Give the extent of all white blood cells.
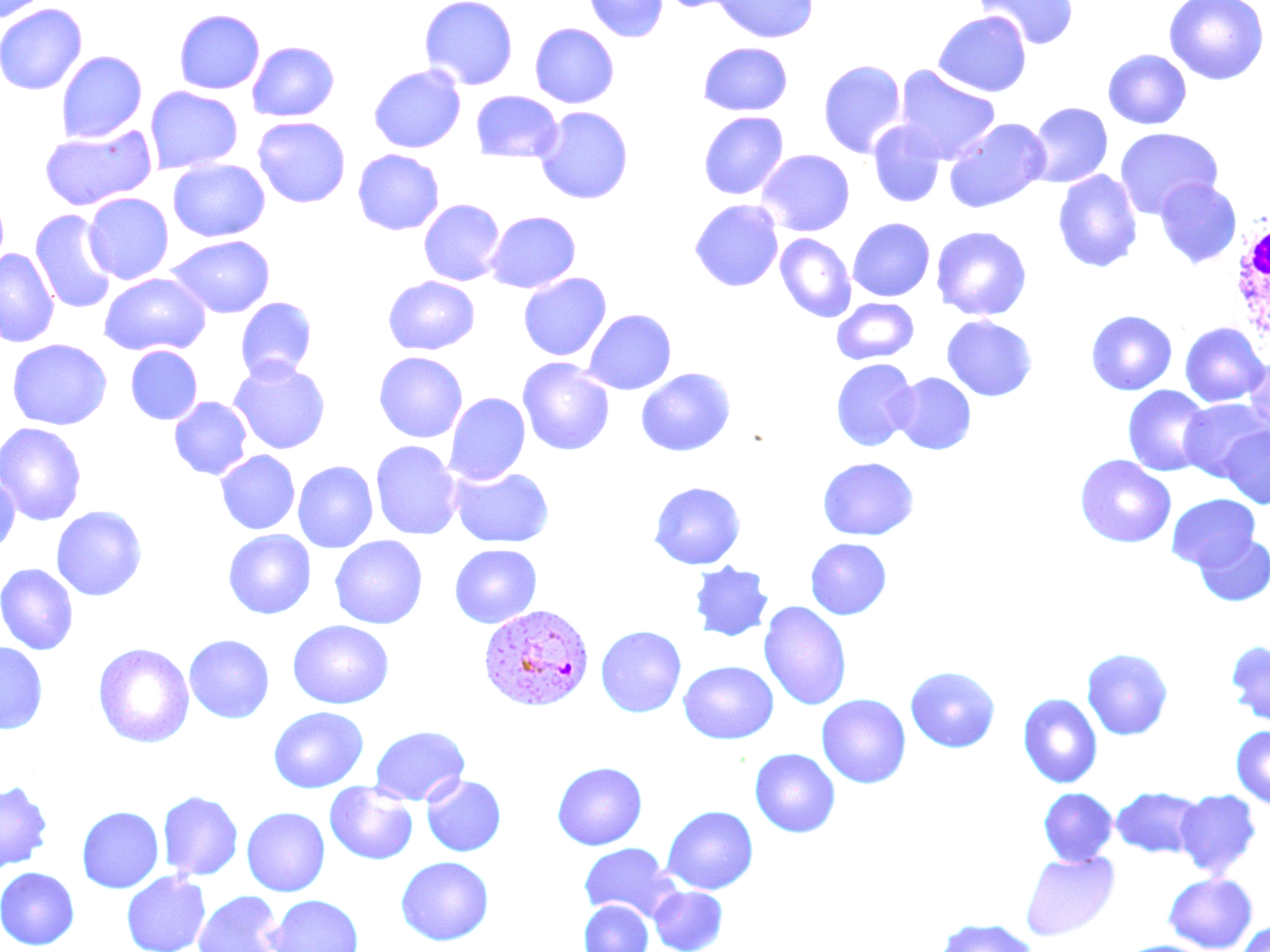

Approximate bounding boxes as (x1,y1)-(x2,y2) corner pairs in pixels.
White blood cells: (1231,212)-(1270,349).

Plasmodium vivax-infected red blood cell locations: (478,605)-(595,714). Uninfected red blood cell locations: (1,0)-(51,24), (420,0)-(518,90), (583,0)-(669,42), (656,0)-(750,13), (712,0)-(819,43), (974,0)-(1080,50), (1164,0)-(1268,86), (0,4)-(88,95), (173,9)-(265,95), (933,11)-(1032,97), (529,23)-(620,108), (247,41)-(340,121), (698,42)-(793,116), (1103,49)-(1192,130), (56,50)-(147,143), (818,60)-(907,159), (368,64)-(466,153), (894,65)-(1001,165), (145,86)-(243,174), (471,90)-(562,161), (1027,102)-(1113,188), (534,106)-(634,205), (698,111)-(789,200), (252,116)-(350,208), (944,117)-(1051,213), (867,121)-(946,208), (39,125)-(157,211), (1115,127)-(1222,220), (352,149)-(445,235), (756,149)-(855,236), (168,159)-(270,242), (1052,169)-(1143,273), (1155,178)-(1242,268), (83,193)-(173,283), (419,199)-(505,286), (689,199)-(784,292), (30,210)-(117,314), (485,210)-(581,294), (848,217)-(935,301), (931,225)-(1032,321), (775,233)-(857,322), (166,235)-(275,319), (0,249)-(59,348), (518,272)-(612,361), (98,273)-(211,357), (384,276)-(480,355), (235,297)-(317,381), (832,298)-(919,365), (582,309)-(676,395), (1086,310)-(1177,395), (941,315)-(1038,402), (1179,322)-(1269,407), (7,338)-(112,430), (126,346)-(203,425), (373,351)-(468,443), (1243,354)-(1270,441), (517,358)-(614,456), (830,358)-(919,451), (229,359)-(331,455), (636,367)-(736,457), (890,372)-(976,455), (1123,386)-(1213,477), (445,393)-(530,485), (170,396)-(252,480), (1179,397)-(1269,482), (0,422)-(87,526), (1219,425)-(1270,509), (370,440)-(462,540), (215,450)-(300,534), (1074,454)-(1176,548), (817,456)-(919,541), (293,460)-(379,553), (449,466)-(554,548), (0,469)-(20,556), (649,481)-(746,569), (1167,494)-(1260,570), (51,505)-(147,601), (223,529)-(315,619), (1194,532)-(1270,606), (329,536)-(428,629), (805,538)-(892,620), (449,544)-(542,628), (688,561)-(774,641), (1,563)-(78,655), (758,601)-(852,711), (288,620)-(394,709), (595,625)-(686,717), (184,634)-(274,724), (0,641)-(49,735), (1226,641)-(1270,725), (93,642)-(195,749), (1081,648)-(1174,741), (678,661)-(778,744), (905,665)-(1001,753), (816,694)-(911,788), (1018,694)-(1103,789), (268,706)-(368,793), (370,725)-(470,806), (1231,725)-(1270,808), (749,748)-(840,837), (552,761)-(647,850), (421,775)-(506,856), (0,780)-(54,872), (325,782)-(418,865), (1111,786)-(1204,859), (1038,787)-(1117,866), (1175,789)-(1262,879), (158,790)-(243,880), (661,805)-(758,895), (77,806)-(163,893), (241,807)-(330,897), (579,842)-(680,922), (1020,851)-(1119,941), (395,856)-(493,945), (0,867)-(80,949), (122,871)-(211,952), (1163,872)-(1258,952), (649,886)-(728,952), (193,890)-(286,952), (265,894)-(364,952), (579,900)-(653,952), (932,918)-(1041,952), (1235,919)-(1270,952), (1118,939)-(1213,952). Slide-level diagnosis: Plasmodium vivax. 1000x magnification. Image is 1270×952 pixels. May-Grünwald-Giemsa stain. Thin blood film. Optical microscopy. Single field of view.